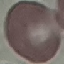 Result: negative for malaria parasites. Acquired by smartphone through the microscope eyepiece. Thin blood smear. Cell patch, automatically extracted from a larger field of view and resized to 64 × 64 pixels. Giemsa stain.